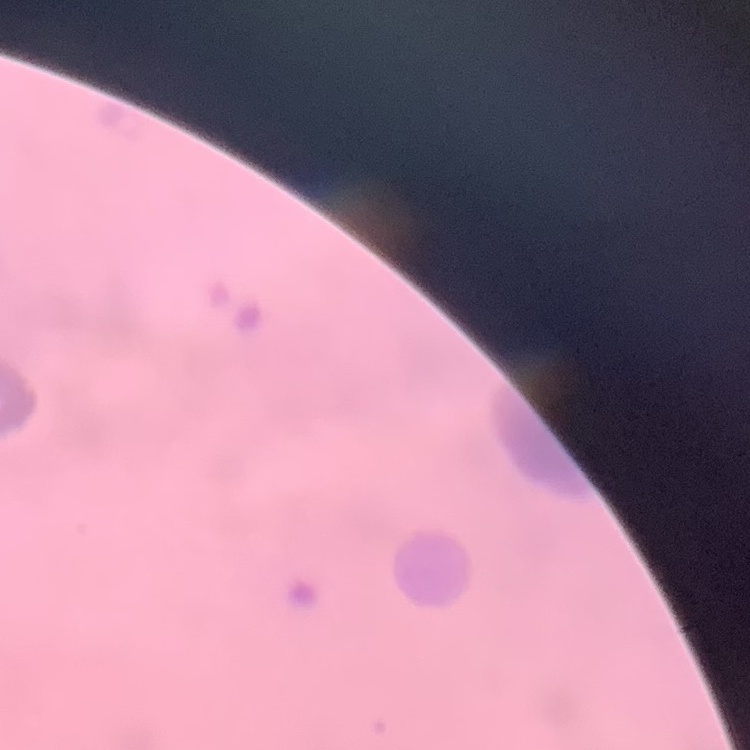
Summary:
  - Red blood cell morphology: rouleaux formation
  - Stain: Field's or Giemsa
  - Image type: square crop of a larger photomicrograph
  - Preparation: thin peripheral smear